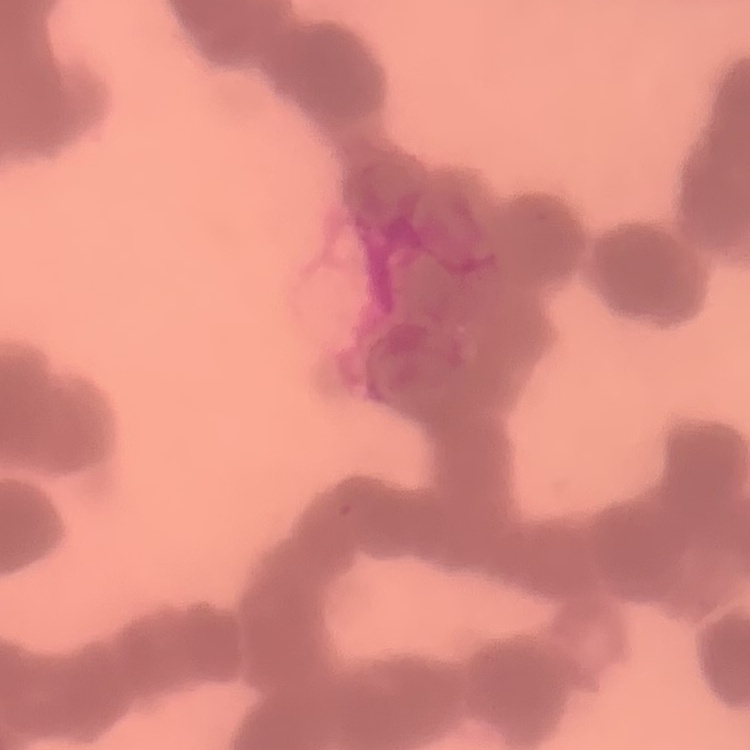 The erythrocytes exhibit rouleaux formation. Stained with either Field's or Giemsa. Square crop of a larger photomicrograph. Thin blood smear.